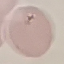

Malaria status: uninfected. Giemsa stain. Thin blood smear. Photographed with a smartphone camera at the microscope eyepiece. Automatically extracted cell patch, resized to 64 × 64 pixels.